Comment on the morphology of the red blood cells.
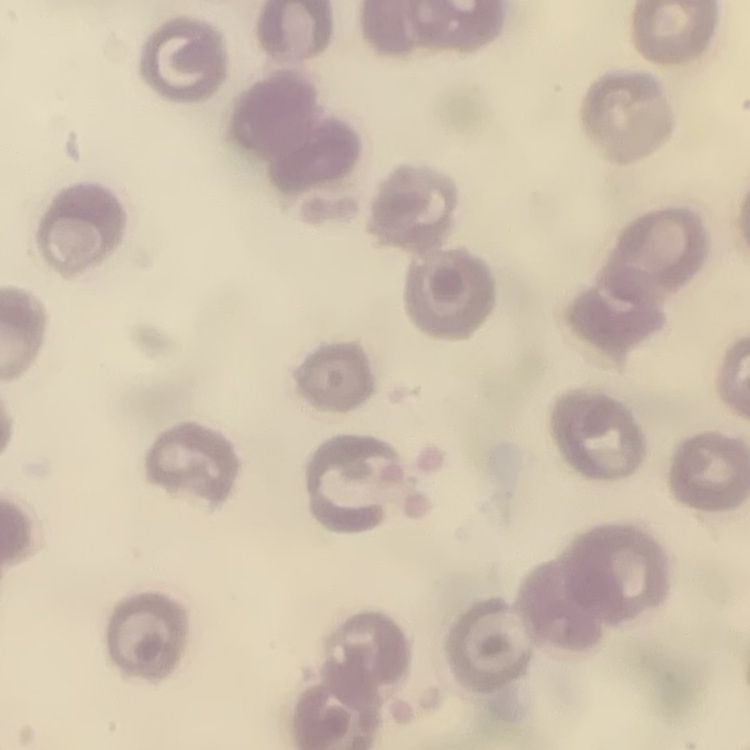

No rouleaux formation.

Thin blood film. Stained with either Field's or Giemsa. Square crop of a larger photomicrograph.